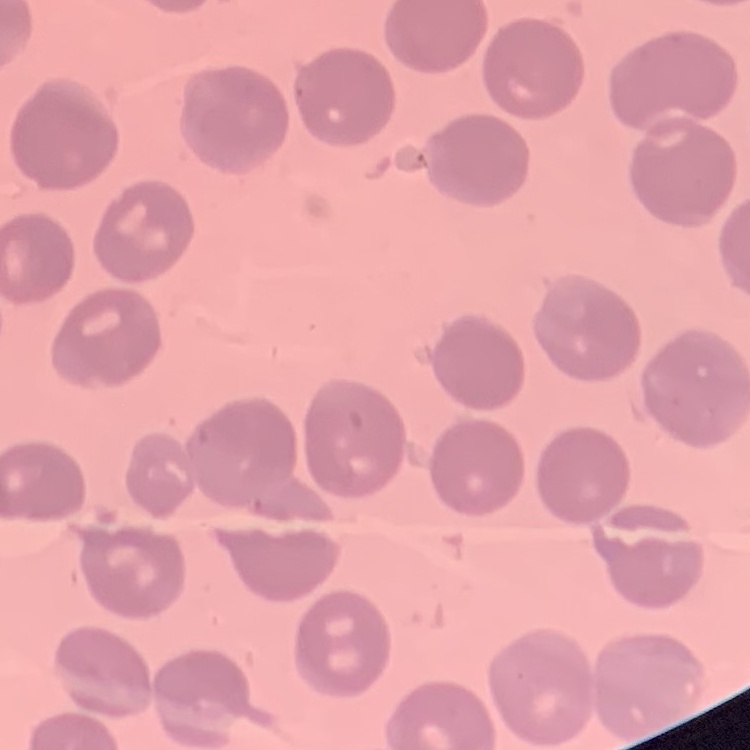

{
  "erythrocyte_morphology": "no rouleaux formation",
  "stain": "Field's or Giemsa",
  "image_type": "one tile cut from a larger photomicrograph",
  "preparation": "thin blood film"
}